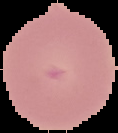 Image is 118×133 pixels. From a thin blood film. Result: no malaria parasites detected. Cell region segmented out of the field of view; the surrounding area is masked to black.